Assess the morphology of the red blood cells.
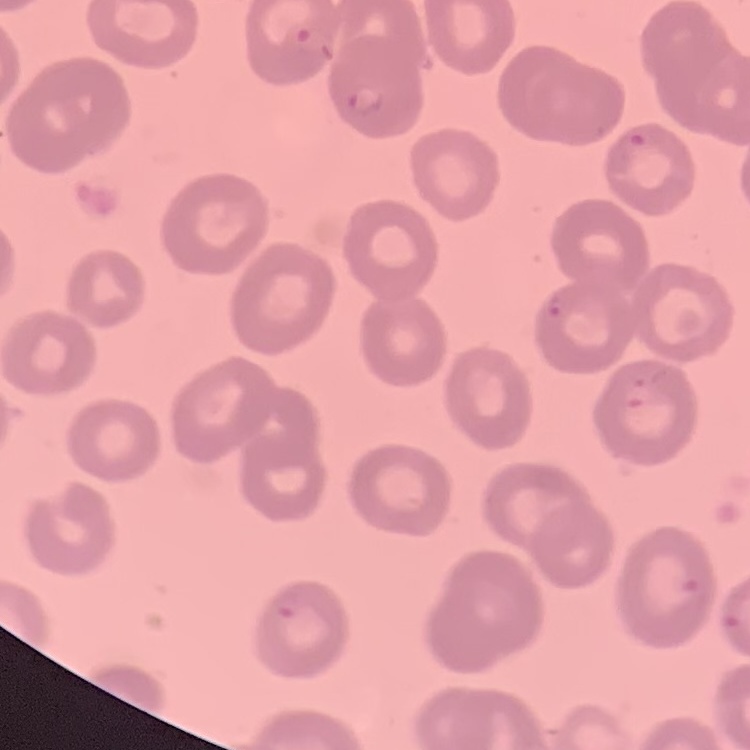

They show no rouleaux formation.

Summary:
  - Stain: Field's or Giemsa
  - Preparation: thin blood film
  - Image type: square crop of a larger photomicrograph